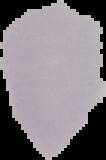
result: no malaria parasites seen
image_size: 106×160 pixels
image_type: segmented cell region with the area outside set to black
preparation: thin blood smear